Describe the morphology of the red blood cells.
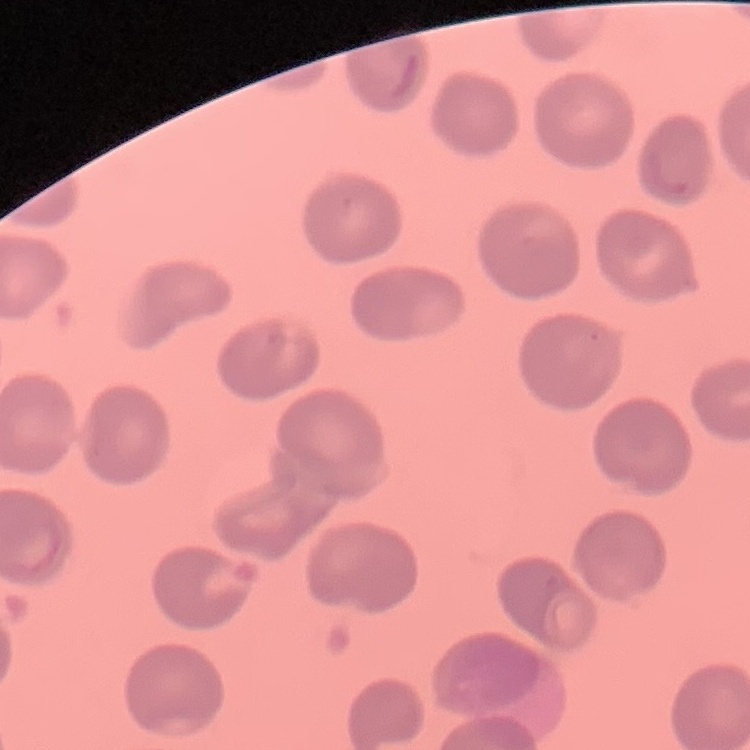

They show no rouleaux formation.

Summary:
  - Image type: square crop of a larger photomicrograph
  - Stain: Field's or Giemsa
  - Preparation: thin peripheral smear